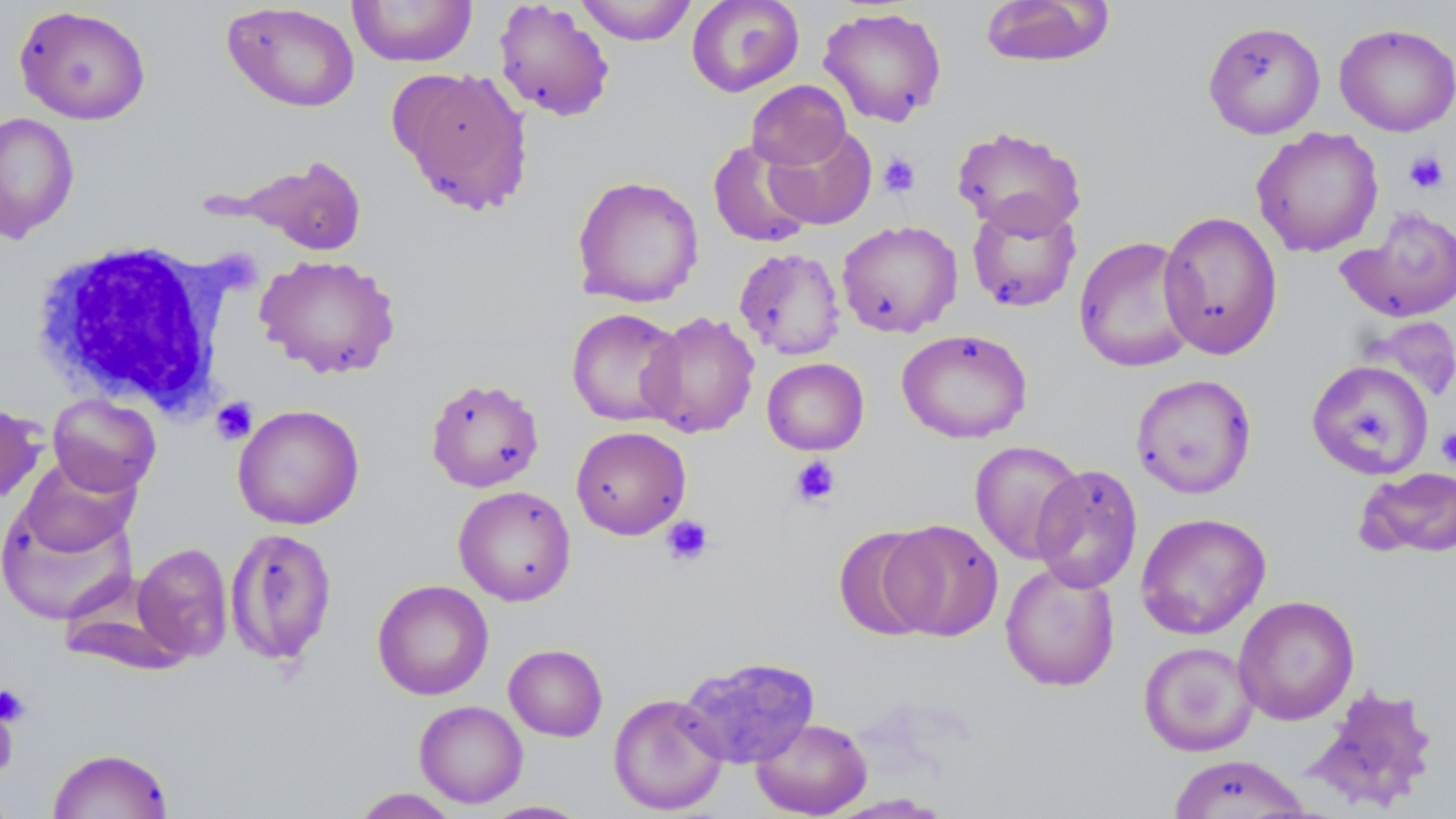
Summary:
  - Coordinate format: approximate bounding boxes as named x1/y1/x2/y2 corners in pixels
  - Platelet locations: (x1=1404, y1=151, x2=1449, y2=194), (x1=877, y1=153, x2=921, y2=197), (x1=211, y1=397, x2=257, y2=445), (x1=1436, y1=428, x2=1456, y2=469), (x1=789, y1=456, x2=840, y2=508), (x1=660, y1=514, x2=713, y2=567), (x1=0, y1=684, x2=31, y2=726), (x1=0, y1=695, x2=20, y2=777)
  - White blood cell locations: (x1=28, y1=238, x2=240, y2=415)
  - Uninfected red blood cell locations: (x1=347, y1=0, x2=478, y2=67), (x1=575, y1=0, x2=696, y2=45), (x1=686, y1=0, x2=804, y2=97), (x1=979, y1=0, x2=1115, y2=68), (x1=493, y1=1, x2=616, y2=122), (x1=221, y1=2, x2=360, y2=113), (x1=14, y1=4, x2=152, y2=125), (x1=817, y1=6, x2=947, y2=127), (x1=1202, y1=21, x2=1326, y2=139), (x1=1334, y1=22, x2=1456, y2=137), (x1=393, y1=67, x2=534, y2=215), (x1=746, y1=80, x2=851, y2=170), (x1=0, y1=112, x2=80, y2=244), (x1=764, y1=124, x2=877, y2=230), (x1=951, y1=125, x2=1087, y2=238), (x1=1251, y1=127, x2=1384, y2=257), (x1=708, y1=139, x2=817, y2=249), (x1=227, y1=155, x2=370, y2=256), (x1=571, y1=175, x2=704, y2=308), (x1=966, y1=199, x2=1082, y2=313), (x1=1337, y1=206, x2=1456, y2=323), (x1=1159, y1=210, x2=1283, y2=360), (x1=836, y1=220, x2=963, y2=338), (x1=1073, y1=235, x2=1200, y2=373), (x1=734, y1=247, x2=846, y2=361), (x1=254, y1=254, x2=401, y2=379), (x1=566, y1=307, x2=686, y2=427), (x1=639, y1=311, x2=760, y2=438), (x1=896, y1=328, x2=1032, y2=444), (x1=762, y1=358, x2=869, y2=455), (x1=1306, y1=359, x2=1434, y2=479), (x1=1130, y1=374, x2=1257, y2=499), (x1=425, y1=376, x2=545, y2=493), (x1=47, y1=393, x2=161, y2=497), (x1=0, y1=403, x2=47, y2=506), (x1=232, y1=403, x2=365, y2=530), (x1=570, y1=426, x2=691, y2=540), (x1=969, y1=440, x2=1085, y2=564), (x1=15, y1=454, x2=141, y2=558), (x1=1030, y1=464, x2=1143, y2=593), (x1=1356, y1=466, x2=1456, y2=559), (x1=453, y1=485, x2=576, y2=606), (x1=0, y1=493, x2=138, y2=626), (x1=1135, y1=512, x2=1271, y2=639), (x1=881, y1=519, x2=1004, y2=641), (x1=833, y1=525, x2=939, y2=641), (x1=224, y1=526, x2=338, y2=668), (x1=132, y1=542, x2=233, y2=662), (x1=1000, y1=562, x2=1121, y2=692), (x1=371, y1=579, x2=494, y2=700), (x1=58, y1=586, x2=191, y2=676), (x1=1233, y1=595, x2=1359, y2=725), (x1=1139, y1=642, x2=1259, y2=757), (x1=504, y1=643, x2=608, y2=741), (x1=678, y1=656, x2=820, y2=769), (x1=1303, y1=682, x2=1441, y2=812), (x1=607, y1=693, x2=729, y2=815), (x1=414, y1=700, x2=528, y2=808), (x1=751, y1=717, x2=872, y2=818), (x1=47, y1=747, x2=175, y2=819), (x1=1168, y1=754, x2=1312, y2=818), (x1=350, y1=788, x2=461, y2=818), (x1=481, y1=800, x2=591, y2=818)
  - Slide-level diagnosis: negative for blood parasites
  - Preparation: thin blood film
  - Magnification: 1000x
  - Stain: May-Grünwald-Giemsa
  - Modality: light microscopy
  - Field of view: single
  - Image size: 1456×819 pixels